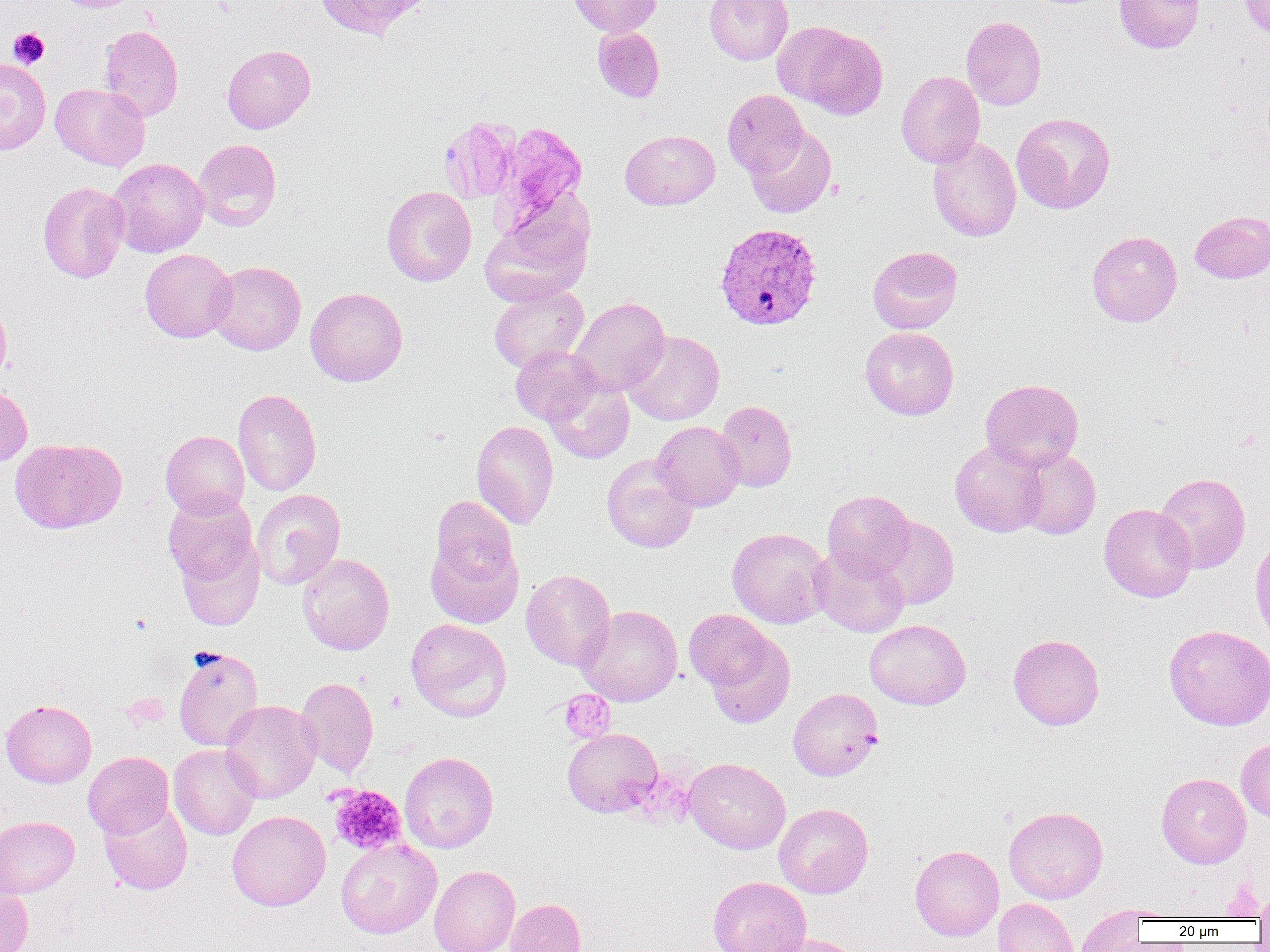

Summary:
  - Coordinate format: approximate bounding boxes as (x1,y1)-(x2,y2) corner pairs in pixels
  - Platelet locations: (8,27)-(50,68), (558,689)-(615,743), (328,784)-(407,856), (1219,881)-(1265,919)
  - Plasmodium vivax-infected red blood cell locations: (714,223)-(823,331)
  - Uninfected red blood cell locations: (52,0)-(146,12), (311,0)-(430,39), (566,0)-(662,37), (705,0)-(793,64), (1115,0)-(1204,53), (1239,0)-(1270,39), (961,16)-(1046,110), (99,24)-(184,122), (789,25)-(887,118), (592,26)-(665,103), (222,44)-(315,133), (0,58)-(51,155), (896,70)-(985,168), (50,83)-(150,171), (723,89)-(809,178), (1011,112)-(1115,214), (439,117)-(520,203), (492,119)-(589,234), (745,125)-(836,218), (620,129)-(720,210), (927,136)-(1021,242), (194,138)-(282,231), (106,157)-(209,257), (37,181)-(129,283), (382,185)-(476,286), (481,200)-(594,305), (1190,210)-(1270,283), (1087,231)-(1182,327), (868,246)-(963,334), (139,248)-(236,342), (207,261)-(306,355), (488,284)-(588,374), (305,287)-(408,386), (0,293)-(12,384), (570,296)-(670,396), (860,327)-(959,420), (623,330)-(724,425), (511,345)-(601,426), (544,376)-(634,464), (980,378)-(1083,472), (0,384)-(33,466), (233,388)-(321,496), (714,400)-(797,492), (471,420)-(559,529), (651,421)-(745,511), (161,430)-(249,519), (10,438)-(126,533), (950,439)-(1047,537), (1016,449)-(1101,539), (601,454)-(699,553), (1154,473)-(1250,573), (251,489)-(345,590), (823,490)-(915,580), (163,492)-(258,589), (430,496)-(518,589), (1099,504)-(1196,603), (868,516)-(959,610), (726,527)-(831,628), (426,534)-(523,628), (176,538)-(264,631), (809,544)-(910,637), (297,553)-(394,655), (521,569)-(615,671), (577,605)-(682,706), (683,609)-(776,692), (406,618)-(511,721), (865,619)-(971,709), (1163,624)-(1270,730), (703,630)-(796,730), (1008,634)-(1105,730), (173,647)-(263,751), (295,676)-(379,777), (788,688)-(883,780), (0,699)-(97,788), (220,700)-(321,803), (563,728)-(662,817), (1236,738)-(1270,822), (168,744)-(262,840), (83,751)-(174,839), (399,751)-(499,853), (684,757)-(790,854), (1156,773)-(1251,869), (99,799)-(192,896), (774,803)-(873,898), (1003,806)-(1108,904), (227,810)-(331,911), (0,816)-(79,899), (336,839)-(442,938), (909,845)-(1004,941), (429,865)-(520,952), (708,875)-(811,952), (1255,886)-(1270,926), (0,889)-(34,952), (505,898)-(586,952), (993,898)-(1079,952), (1085,905)-(1179,922), (1075,906)-(1150,951), (761,933)-(868,952)
  - Slide-level diagnosis: Plasmodium vivax
  - Modality: optical microscopy
  - Preparation: thin blood film
  - Image size: 1270×952 pixels
  - Magnification: 1000x
  - Field of view: one of a larger specimen